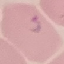

Summary:
  - Result: malaria parasites identified
  - Image type: cell patch, automatically extracted from a larger field of view and resized to 64 × 64 pixels
  - Preparation: thin blood smear
  - Capture: smartphone camera at the microscope eyepiece
  - Stain: Giemsa